Report the malaria status of this cell.
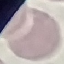

Uninfected.

preparation = thin blood smear
stain = Giemsa
capture = smartphone through the microscope eyepiece
image type = automatically extracted cell patch, resized to 64 × 64 pixels